Locate every Plasmodium ovale-infected red blood cell.
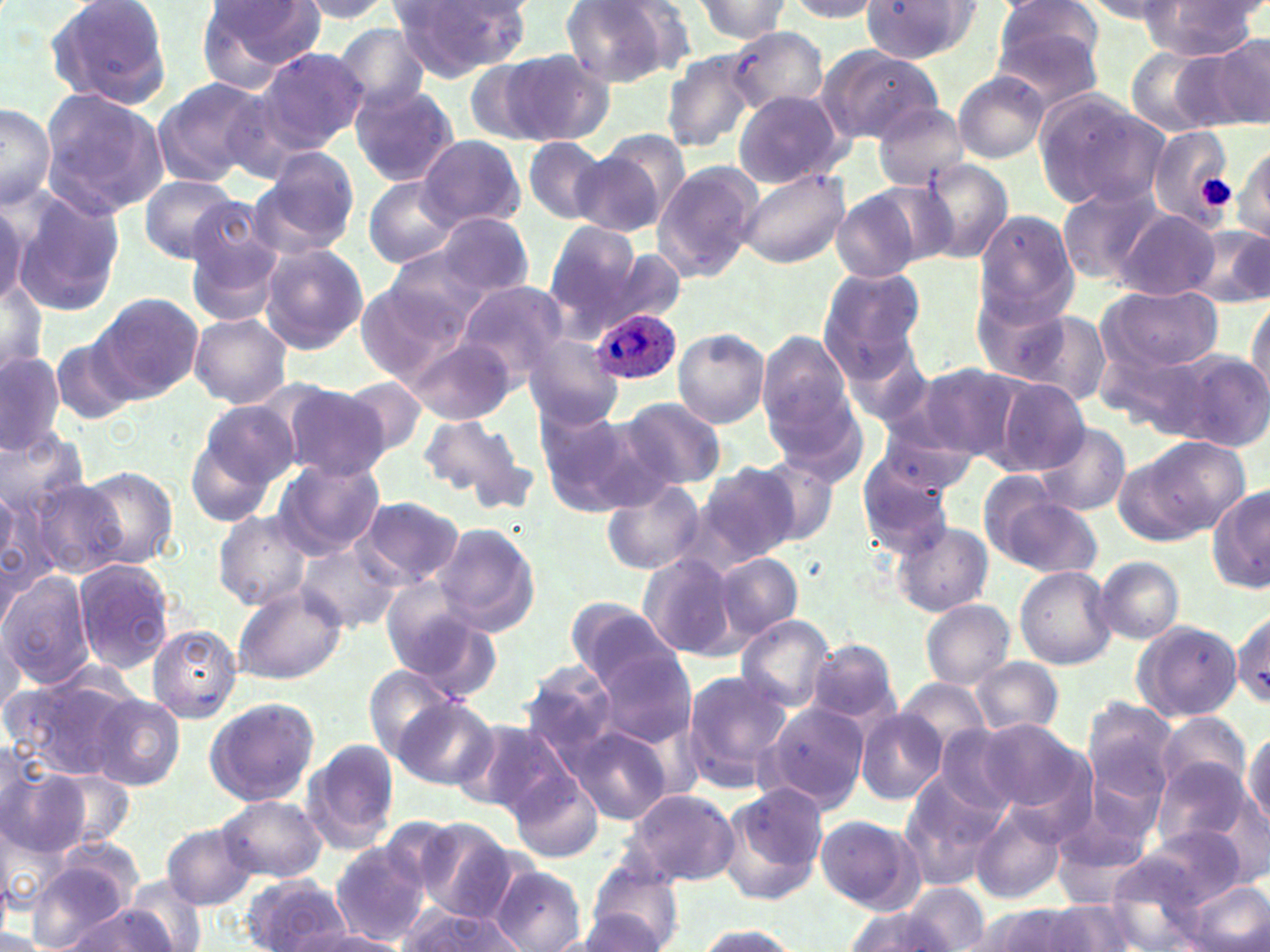

Approximate bounding boxes as (x1,y1)-(x2,y2) corner pairs in pixels.
Plasmodium ovale-infected red blood cells: (587,307)-(683,385).

{
  "slide_level_diagnosis": "Plasmodium ovale",
  "platelet_locations": "approximate bounding boxes as (x1,y1)-(x2,y2) corner pairs in pixels: (1195,175)-(1237,213)",
  "preparation": "thin blood film",
  "modality": "light microscopy",
  "field_of_view": "single",
  "stain": "May-Grünwald-Giemsa",
  "magnification": "1000x",
  "uninfected_red_blood_cell_locations": "approximate bounding boxes as (x1,y1)-(x2,y2) corner pairs in pixels: (43,0)-(174,111), (195,0)-(326,90), (292,0)-(398,22), (561,0)-(684,87), (864,0)-(982,63), (991,0)-(1107,98), (1136,0)-(1266,59), (390,1)-(533,82), (689,1)-(794,42), (785,1)-(885,23), (1076,1)-(1183,22), (332,23)-(432,113), (728,27)-(828,114), (1210,33)-(1270,131), (818,45)-(943,145), (254,47)-(368,152), (1126,47)-(1228,136), (504,49)-(613,146), (660,50)-(763,155), (462,59)-(553,146), (954,72)-(1048,162), (151,77)-(269,186), (350,83)-(459,187), (38,89)-(169,216), (733,90)-(844,188), (1035,92)-(1167,210), (0,101)-(56,209), (872,101)-(971,192), (1147,128)-(1235,229), (415,133)-(526,232), (521,138)-(608,224), (1233,142)-(1269,241), (569,148)-(671,240), (251,152)-(358,256), (917,161)-(1017,263), (653,163)-(763,281), (734,167)-(850,269), (137,174)-(242,264), (358,177)-(464,268), (1056,184)-(1166,287), (6,186)-(129,318), (830,186)-(937,282), (0,197)-(27,316), (181,205)-(288,324), (1114,209)-(1220,300), (974,210)-(1080,324), (431,212)-(534,298), (1181,221)-(1270,307), (544,222)-(641,329), (257,243)-(368,355), (385,249)-(495,339), (607,249)-(688,328), (820,267)-(926,370), (0,273)-(46,381), (355,274)-(473,382), (454,281)-(569,386), (968,285)-(1088,388), (1099,286)-(1221,376), (1247,292)-(1270,401), (91,293)-(203,401), (1001,305)-(1114,408), (189,313)-(292,408), (672,328)-(770,428), (525,334)-(625,429), (757,334)-(853,443), (405,336)-(515,425), (50,338)-(134,424), (1171,350)-(1270,449), (0,352)-(64,456), (911,363)-(1032,463), (338,375)-(429,460), (995,378)-(1089,475), (279,382)-(392,481), (768,384)-(866,484), (620,397)-(726,489), (184,401)-(293,525), (534,405)-(651,517), (418,413)-(526,504), (872,418)-(980,504), (1032,422)-(1132,518), (0,427)-(91,529), (1124,436)-(1247,542), (854,451)-(958,557), (752,456)-(841,549), (273,459)-(385,559), (694,462)-(798,565), (75,465)-(180,569), (601,476)-(706,576), (27,478)-(129,579), (0,484)-(58,609), (983,486)-(1100,579), (1209,486)-(1270,594), (352,497)-(466,589), (216,511)-(312,610), (432,521)-(541,636), (893,521)-(994,616), (296,543)-(401,633), (637,552)-(741,658), (713,552)-(802,640), (1095,556)-(1185,644), (73,558)-(175,672), (1014,565)-(1117,669), (0,571)-(95,686), (232,586)-(347,686), (381,586)-(498,694), (565,597)-(676,687), (920,599)-(1014,688), (1232,610)-(1268,707), (735,616)-(834,711), (1130,620)-(1243,722), (147,623)-(243,722), (0,630)-(24,718), (805,638)-(901,725), (592,649)-(697,749), (974,656)-(1063,736), (518,661)-(626,763), (363,665)-(461,762), (679,667)-(793,787), (3,669)-(138,782), (897,678)-(990,753), (390,692)-(497,789), (88,694)-(185,790), (202,696)-(320,808), (1081,698)-(1179,803), (762,699)-(867,810), (856,710)-(946,803), (1157,711)-(1252,796), (460,720)-(573,818), (977,721)-(1085,815), (1245,724)-(1270,829), (567,725)-(672,826), (928,725)-(1025,823), (0,738)-(43,835), (302,738)-(400,852), (509,742)-(666,847), (1152,760)-(1255,855), (0,761)-(86,861), (41,770)-(133,853), (510,772)-(603,862), (897,779)-(1003,890), (720,783)-(828,903), (626,788)-(740,886), (219,795)-(326,882), (1052,797)-(1156,900), (970,803)-(1067,904), (813,815)-(924,913), (410,818)-(523,923), (162,823)-(259,911), (1124,824)-(1253,913), (329,845)-(430,945), (25,858)-(140,948), (1102,862)-(1215,951), (584,863)-(687,951), (491,864)-(587,951), (124,873)-(208,952), (241,874)-(352,951), (1181,877)-(1269,952), (897,884)-(988,951), (398,898)-(529,952), (1040,899)-(1139,952), (60,905)-(179,951), (957,906)-(1065,952), (840,907)-(968,952), (563,910)-(673,951), (694,922)-(801,952), (302,930)-(414,952)",
  "image_size": "1270×952 pixels"
}